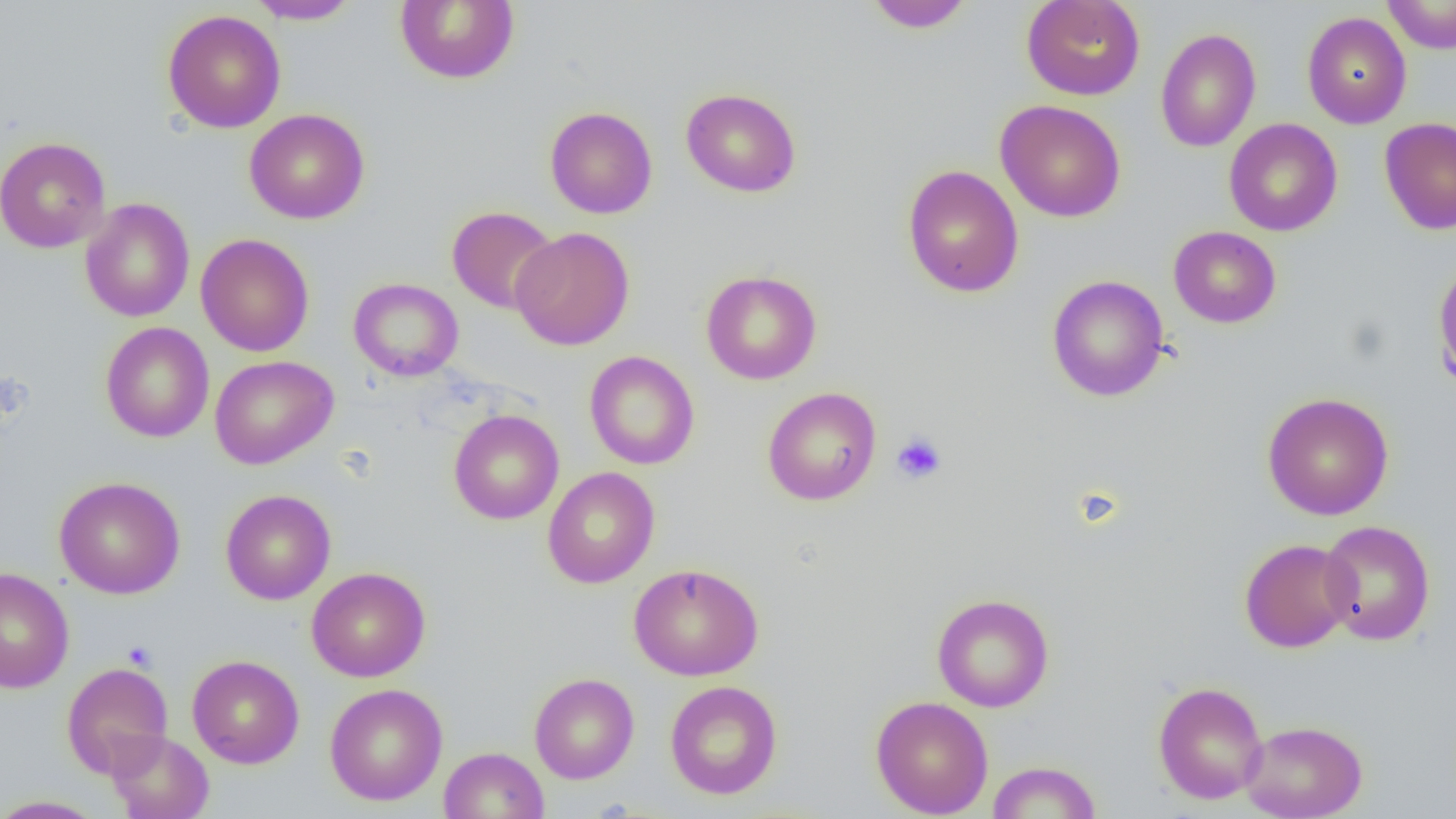
slide-level diagnosis = negative for blood parasites
platelet locations = approximate bounding boxes as (x1, y1, x2, y2) in pixels: (890, 432, 947, 485), (122, 640, 157, 671)
preparation = thin blood smear
image size = 1456×819 pixels
field of view = single
uninfected red blood cell locations = approximate bounding boxes as (x1, y1, x2, y2) in pixels: (394, 0, 519, 85), (1021, 0, 1146, 100), (247, 1, 362, 24), (862, 1, 975, 32), (1384, 1, 1456, 53), (162, 10, 286, 133), (1302, 12, 1412, 129), (1155, 28, 1261, 153), (680, 87, 802, 197), (995, 100, 1126, 223), (544, 106, 658, 219), (244, 108, 370, 224), (1379, 117, 1456, 235), (1224, 118, 1343, 236), (0, 136, 111, 253), (902, 165, 1023, 298), (79, 198, 195, 322), (447, 206, 560, 314), (1169, 226, 1281, 328), (510, 227, 635, 350), (195, 233, 314, 357), (1432, 257, 1456, 394), (701, 270, 822, 385), (1047, 275, 1169, 402), (348, 277, 464, 381), (100, 322, 214, 443), (584, 351, 700, 470), (210, 355, 338, 469), (762, 387, 881, 506), (1262, 392, 1394, 520), (448, 409, 564, 525), (542, 467, 660, 589), (53, 476, 185, 599), (220, 489, 336, 605), (1319, 520, 1435, 645), (1239, 538, 1357, 653), (628, 562, 764, 681), (306, 566, 431, 682), (0, 567, 74, 693), (931, 593, 1054, 712), (187, 654, 304, 769), (61, 662, 174, 779), (529, 673, 639, 784), (664, 680, 782, 799), (1152, 680, 1268, 805), (324, 683, 448, 806), (870, 695, 994, 818), (1240, 719, 1367, 819), (105, 729, 215, 819), (439, 746, 549, 819), (987, 760, 1102, 818), (0, 795, 109, 818)
magnification = 1000x
modality = light microscopy